Give the position of every Plasmodium parasite.
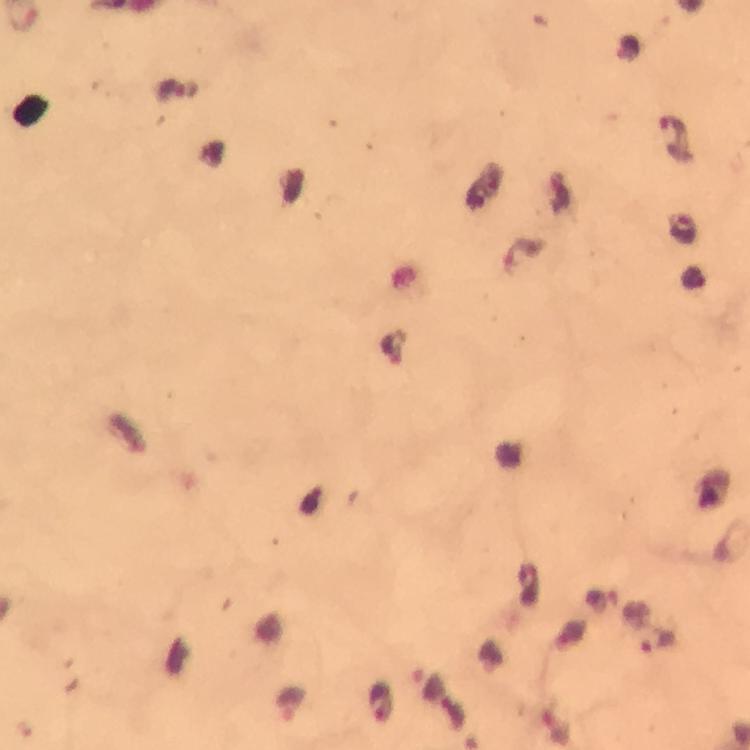

Approximate object centers, in pixels from the top-left corner.
Plasmodium parasites: (x=628, y=48), (x=169, y=90), (x=674, y=131), (x=682, y=228), (x=522, y=253), (x=658, y=640), (x=429, y=683), (x=380, y=701), (x=292, y=704), (x=556, y=728).

stain = Giemsa
context = from a malaria diagnostic workup
preparation = thick smear
magnification = 100x
immersion oil = applied
cropped from = a single field of view
image size = 750×750 pixels
capture = smartphone camera through the microscope